Name the cell type shown.
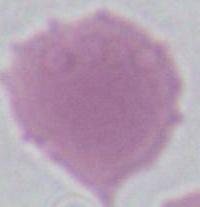

An erythrocyte.

Summary:
  - Modality: photomicrograph
  - Magnification: 1000x